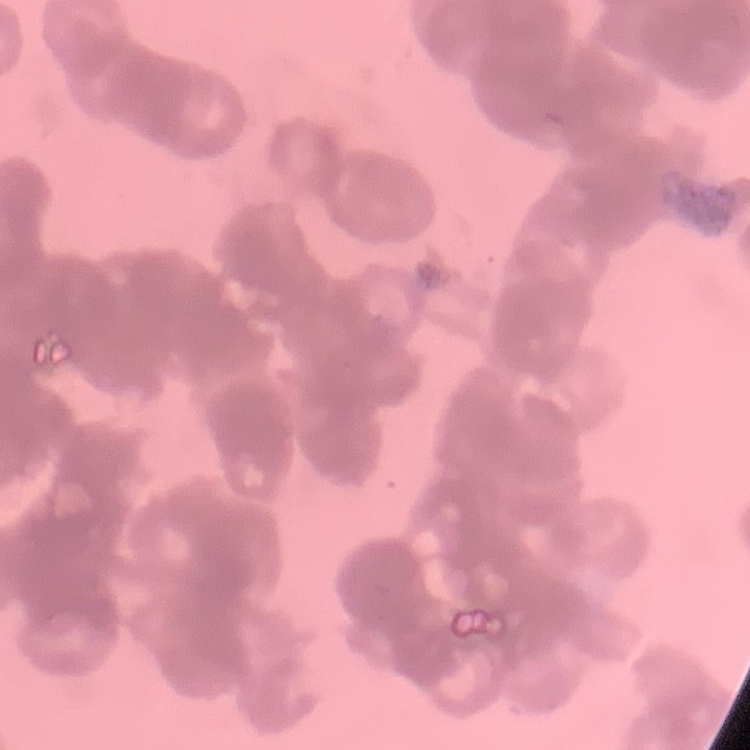

{
  "red_blood_cell_morphology": "rouleaux formation",
  "preparation": "thin peripheral smear",
  "image_type": "one tile cut from a larger photomicrograph",
  "stain": "Field's or Giemsa"
}